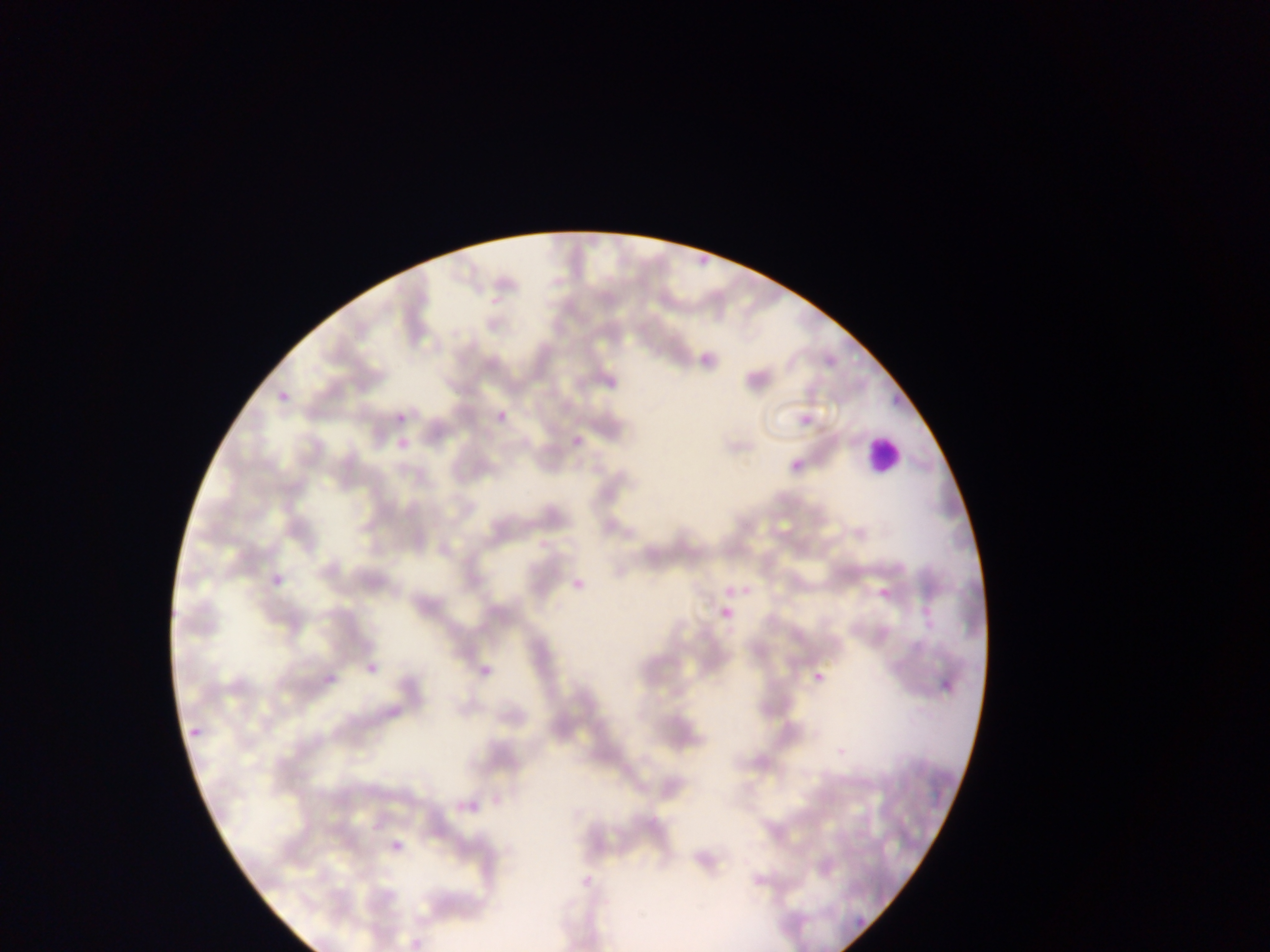
{
  "country": "Ghana",
  "malaria_parasite_locations": "approximate bounding boxes as left top right bottom in pixels: 691 240 728 267; 694 350 716 369; 604 376 625 392; 877 381 916 407; 274 387 292 409; 491 409 510 425; 396 412 407 423; 800 413 813 424; 572 429 598 449; 393 434 415 450; 790 459 803 473; 270 559 293 588; 569 576 590 593; 877 580 893 603; 722 582 743 598; 913 604 932 625; 715 608 734 621; 360 656 384 676; 470 662 493 679; 812 664 829 682; 323 670 341 687; 933 674 962 697; 185 726 205 741; 450 796 496 818; 386 827 407 855; 856 916 866 925",
  "capture": "mobile-phone photograph through a microscope",
  "image_size": "1270×952 pixels",
  "preparation": "thin blood smear",
  "leukocyte_locations": "approximate bounding boxes as left top right bottom in pixels: 863 431 905 475",
  "field_of_view": "single"
}